State which parasite is depicted.
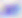
Toxoplasma gondii.

modality = micrograph
magnification = 400x